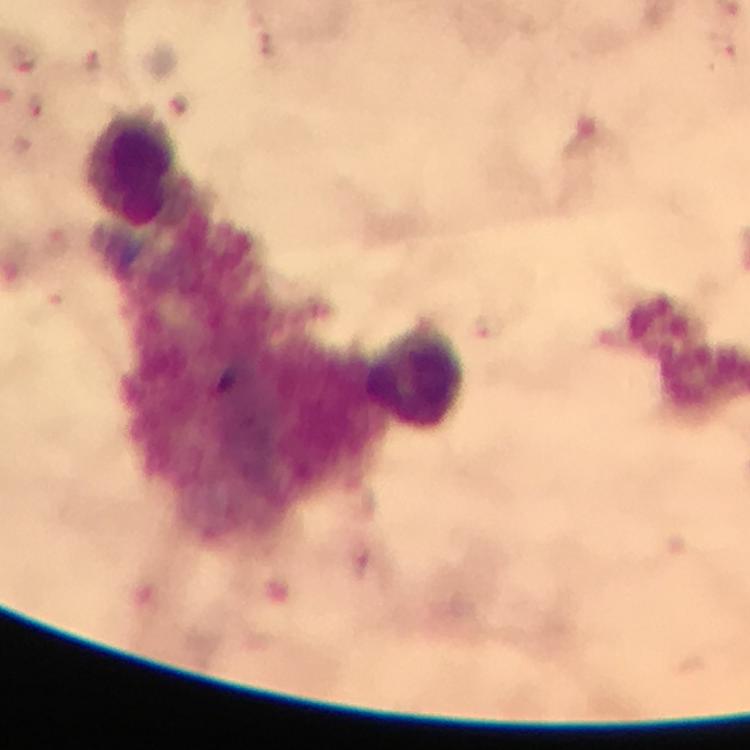

capture = smartphone mounted on the microscope
preparation = thick blood film
magnification = 100x
cropped from = one field of view
leukocyte locations = approximate object centers, in pixels from the top-left corner: (x=131, y=167), (x=414, y=374)
Plasmodium parasite locations = approximate object centers, in pixels from the top-left corner: (x=267, y=42), (x=722, y=45)
context = from a diagnostic examination for malaria
image size = 750×750 pixels
immersion oil = used
stain = Giemsa